Assess this cell for malaria.
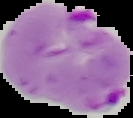
It is parasitized.

The area outside the segmented cell region is set to black. Image is 133×118 pixels. From a thin blood smear.